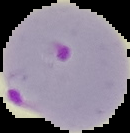

result: Plasmodium parasites detected
image_type: segmented cell region on a black background
preparation: thin blood film
image_size: 130×133 pixels